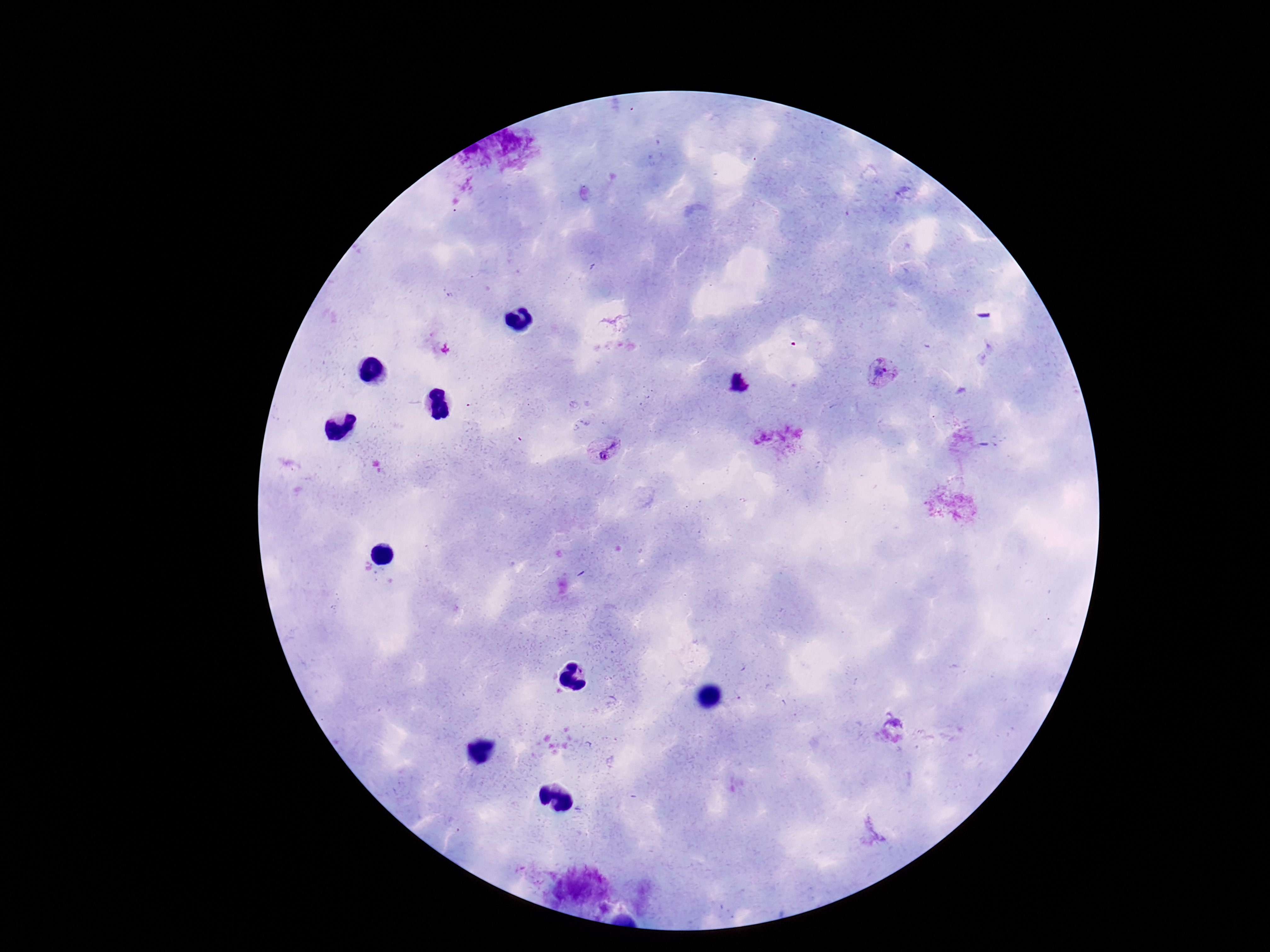 Approximate object centers, in pixels from the top-left corner. Plasmodium parasite locations: (x=881, y=374), (x=777, y=436), (x=603, y=451). Photographed through the microscope eyepiece with a smartphone camera. 100x magnification. Single field of view. Image is 1270×952 pixels. Thick blood smear. Giemsa-stained preparation. Patient malaria status: infected.